State which parasite is depicted.
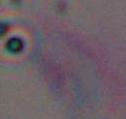

This is Toxoplasma gondii.

magnification = 1000x
modality = photomicrograph